Identify the parasite.
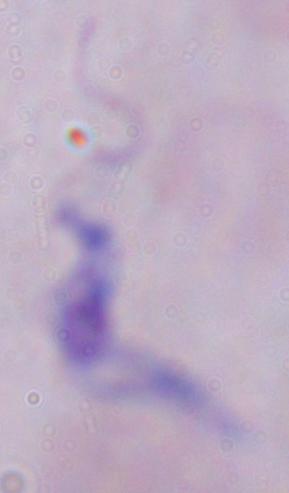

A trypanosome.

Photomicrograph. Captured at 1000x magnification.